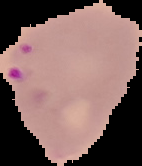

Image is 142×166 pixels. From a thin blood smear. Malaria status: parasitized. The area outside the segmented cell region is set to black.